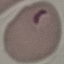
Summary:
  - Malaria status: parasitized
  - Image type: automatically extracted cell patch, resized to 64 × 64 pixels
  - Stain: Giemsa
  - Capture: smartphone through the microscope eyepiece
  - Preparation: thin blood smear